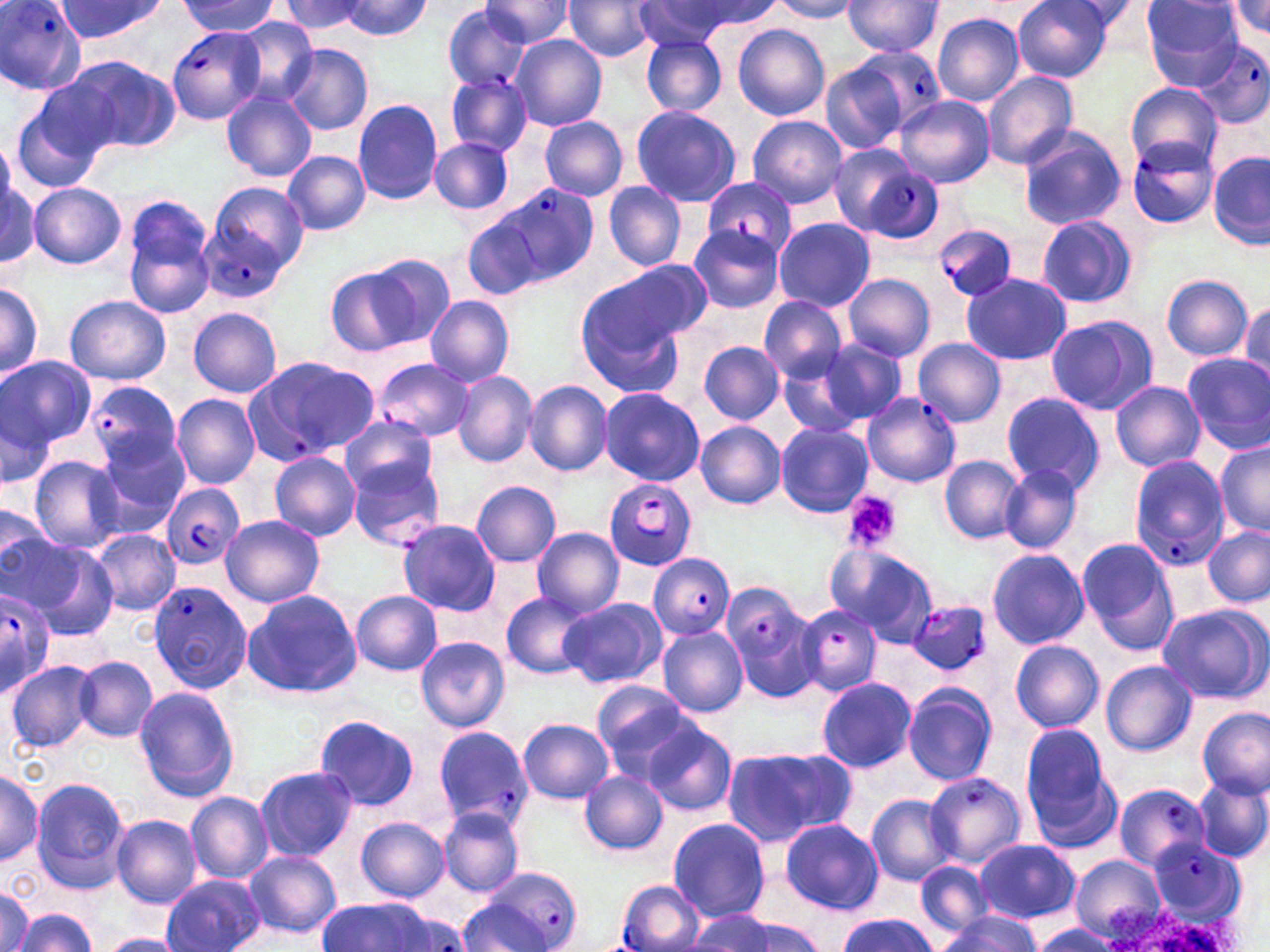
Summary:
  - Coordinate format: approximate bounding boxes as [x1, y1, x2, y2] in pixels
  - Plasmodium falciparum-infected red blood cell locations: [0, 0, 87, 93], [167, 27, 264, 122], [1192, 39, 1270, 128], [845, 45, 946, 136], [446, 72, 531, 156], [1125, 136, 1218, 228], [829, 147, 935, 241], [702, 178, 796, 257], [481, 184, 597, 289], [933, 221, 1021, 301], [190, 226, 285, 300], [244, 355, 381, 464], [373, 359, 475, 441], [86, 380, 183, 476], [861, 393, 960, 488], [1129, 455, 1228, 570], [349, 460, 446, 551], [604, 479, 697, 571], [160, 482, 243, 571], [648, 554, 736, 640], [149, 580, 252, 695], [724, 585, 820, 696], [0, 587, 56, 695], [907, 601, 992, 675], [796, 604, 882, 698], [434, 725, 535, 827], [924, 771, 1026, 867], [1113, 786, 1209, 870], [1148, 838, 1247, 925], [469, 867, 584, 951], [616, 880, 703, 951]
  - Platelet locations: [840, 490, 900, 551]
  - Uninfected red blood cell locations: [177, 0, 280, 37], [282, 0, 370, 35], [480, 0, 577, 47], [1014, 0, 1114, 82], [1229, 0, 1270, 38], [51, 1, 166, 45], [338, 1, 433, 40], [563, 1, 660, 62], [631, 1, 744, 50], [769, 1, 862, 22], [842, 1, 945, 59], [1140, 1, 1243, 87], [442, 4, 534, 93], [931, 13, 1023, 106], [230, 19, 318, 106], [734, 24, 830, 120], [509, 34, 606, 132], [641, 34, 727, 117], [282, 43, 373, 135], [64, 56, 182, 154], [821, 62, 907, 154], [982, 71, 1077, 169], [1126, 85, 1221, 170], [220, 87, 317, 181], [11, 89, 111, 193], [894, 95, 994, 188], [352, 98, 444, 206], [629, 105, 741, 207], [747, 114, 848, 208], [539, 116, 628, 200], [1017, 127, 1126, 229], [429, 136, 514, 216], [282, 150, 371, 234], [1209, 150, 1269, 250], [1, 178, 39, 267], [204, 181, 308, 262], [603, 182, 688, 271], [28, 183, 126, 268], [121, 199, 218, 318], [462, 214, 547, 301], [1036, 214, 1138, 309], [774, 217, 876, 311], [688, 224, 785, 314], [363, 251, 455, 347], [593, 260, 711, 349], [327, 267, 423, 356], [843, 273, 937, 361], [961, 274, 1071, 366], [1162, 275, 1255, 361], [0, 278, 44, 385], [574, 292, 682, 398], [64, 295, 171, 385], [760, 295, 847, 383], [425, 296, 515, 388], [1239, 299, 1270, 387], [188, 308, 282, 397], [1045, 314, 1157, 416], [913, 337, 1005, 427], [820, 339, 909, 425], [698, 341, 784, 423], [1183, 352, 1270, 453], [780, 355, 870, 439], [1, 356, 96, 448], [453, 370, 537, 468], [523, 380, 612, 477], [1110, 381, 1205, 472], [599, 388, 704, 485], [1, 391, 58, 492], [1001, 393, 1106, 495], [171, 394, 260, 490], [342, 415, 438, 500], [695, 421, 786, 509], [775, 422, 872, 516], [94, 435, 190, 538], [1215, 440, 1269, 534], [271, 452, 361, 542], [939, 454, 1026, 546], [27, 455, 126, 553], [999, 465, 1082, 555], [471, 481, 561, 568], [0, 507, 53, 583], [221, 515, 324, 607], [396, 519, 500, 616], [1202, 525, 1269, 607], [532, 526, 625, 618], [90, 528, 180, 617], [1, 529, 83, 613], [24, 540, 120, 640], [1076, 540, 1179, 654], [826, 544, 937, 643], [986, 548, 1089, 650], [242, 589, 361, 700], [350, 591, 443, 676], [502, 591, 595, 679], [558, 598, 665, 689], [1156, 604, 1268, 702], [658, 627, 749, 716], [416, 637, 509, 732], [1010, 641, 1104, 732], [74, 656, 157, 742], [6, 660, 97, 752], [1101, 661, 1197, 755], [816, 677, 917, 772], [592, 681, 695, 773], [902, 684, 997, 785], [135, 687, 239, 801], [1198, 707, 1269, 799], [315, 715, 420, 811], [518, 718, 613, 803], [642, 719, 737, 816], [1021, 725, 1114, 835], [719, 745, 852, 849], [254, 765, 357, 862], [0, 766, 41, 868], [581, 770, 667, 854], [1190, 775, 1270, 863], [30, 778, 130, 894], [185, 791, 272, 883], [866, 794, 959, 886], [439, 806, 526, 896], [112, 814, 201, 908], [356, 818, 450, 901], [669, 819, 769, 922], [779, 819, 883, 914], [974, 839, 1079, 922], [243, 850, 341, 939], [1071, 856, 1164, 941], [914, 861, 994, 938], [163, 873, 265, 952], [0, 886, 32, 952], [316, 897, 436, 952], [455, 900, 548, 948], [1099, 903, 1238, 952], [13, 909, 98, 951], [935, 910, 1044, 950], [690, 911, 821, 952], [836, 913, 937, 951], [1027, 924, 1118, 952], [98, 933, 188, 952]
  - Slide-level diagnosis: Plasmodium falciparum
  - Field of view: single
  - Preparation: thin blood film
  - Modality: optical microscopy
  - Image size: 1270×952 pixels
  - Stain: May-Grünwald-Giemsa
  - Magnification: 1000x